Assess this cell for malaria.
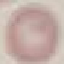
Uninfected.

Giemsa stain. Cell patch, automatically extracted from a larger field of view and resized to 64 × 64 pixels. Thin smear of blood. Acquired by smartphone through the microscope eyepiece.